Describe the morphology of the red blood cells.
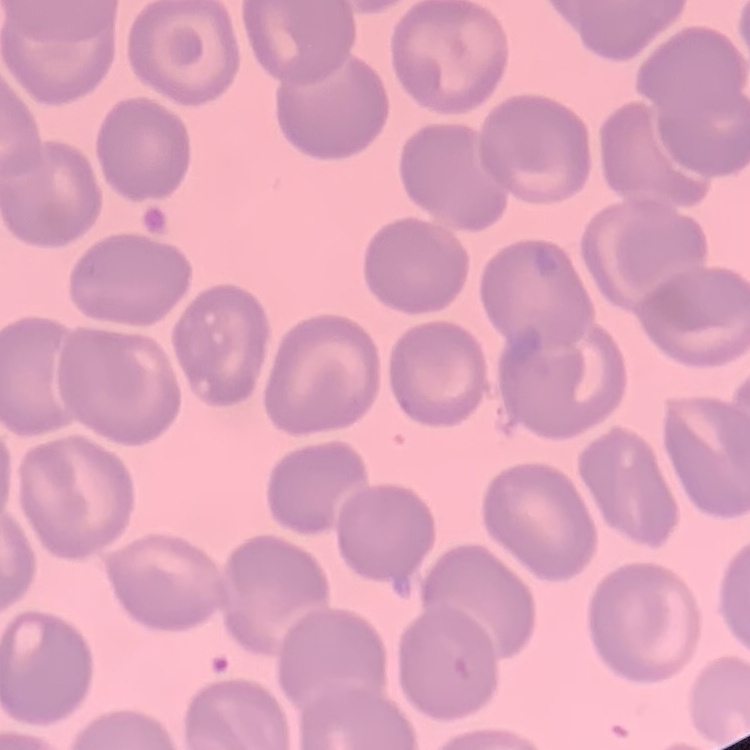
No rouleaux formation.

image type = square crop of a larger photomicrograph
preparation = thin blood film
stain = Field's or Giemsa